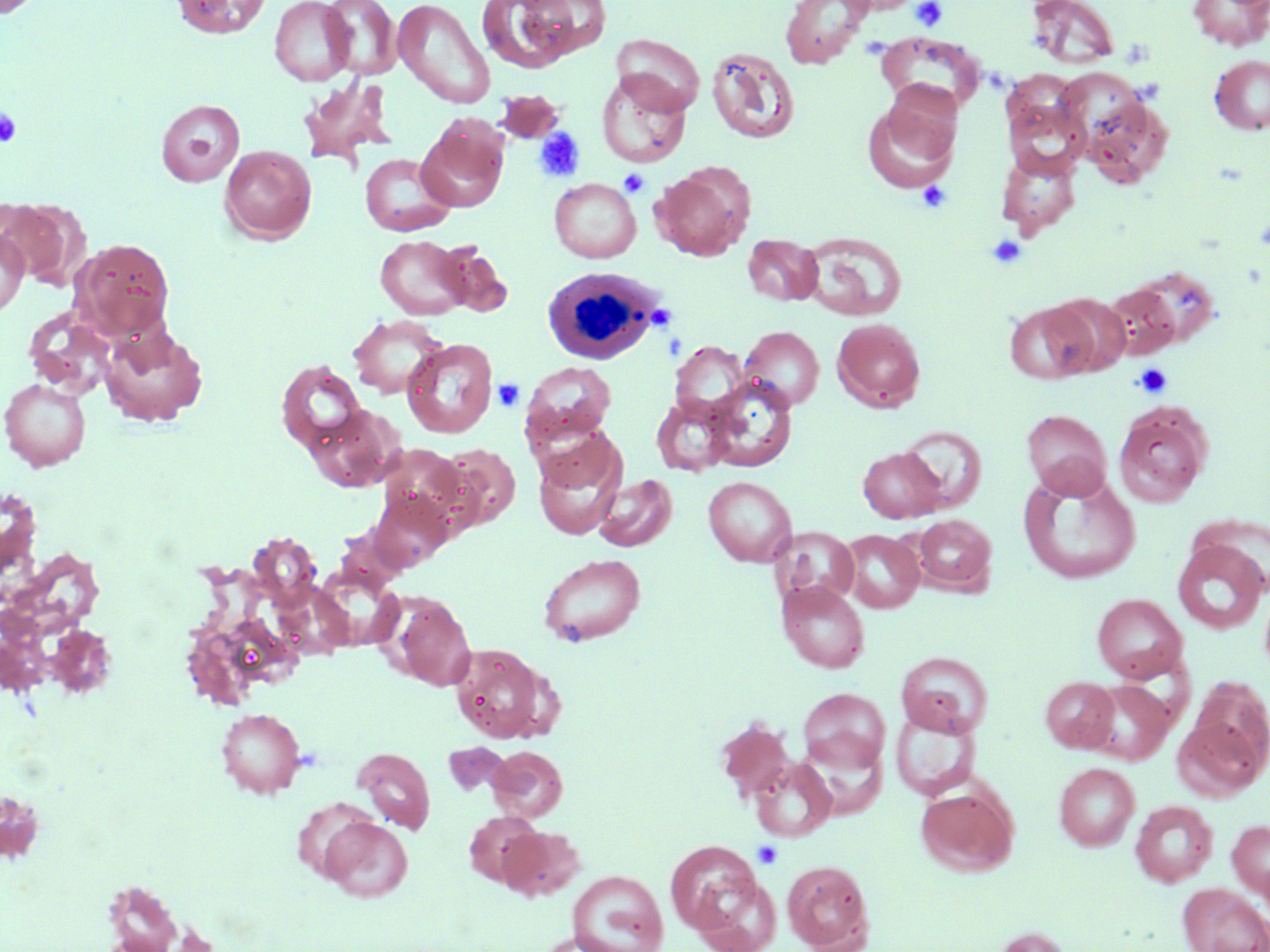

Summary:
  - Coordinate format: approximate bounding boxes as named x1/y1/x2/y2 corners in pixels
  - Uninfected red blood cell locations (subset): (x1=171, y1=0, x2=270, y2=38), (x1=321, y1=0, x2=401, y2=80), (x1=393, y1=0, x2=495, y2=109), (x1=476, y1=0, x2=585, y2=73), (x1=781, y1=0, x2=873, y2=68), (x1=840, y1=0, x2=922, y2=14), (x1=1026, y1=0, x2=1119, y2=70), (x1=1188, y1=0, x2=1270, y2=51), (x1=269, y1=1, x2=355, y2=86), (x1=876, y1=32, x2=983, y2=116), (x1=612, y1=34, x2=704, y2=115), (x1=706, y1=46, x2=800, y2=144), (x1=1209, y1=55, x2=1270, y2=135), (x1=596, y1=70, x2=692, y2=167), (x1=298, y1=76, x2=399, y2=168), (x1=494, y1=90, x2=564, y2=144), (x1=862, y1=92, x2=960, y2=192), (x1=1078, y1=93, x2=1174, y2=188), (x1=1003, y1=97, x2=1088, y2=180), (x1=156, y1=99, x2=245, y2=187), (x1=416, y1=116, x2=509, y2=212), (x1=220, y1=145, x2=316, y2=244), (x1=996, y1=150, x2=1081, y2=239), (x1=360, y1=153, x2=454, y2=237), (x1=651, y1=167, x2=752, y2=260), (x1=550, y1=178, x2=641, y2=263), (x1=0, y1=229, x2=28, y2=317), (x1=801, y1=232, x2=908, y2=321), (x1=375, y1=234, x2=471, y2=319), (x1=743, y1=234, x2=823, y2=305), (x1=72, y1=238, x2=175, y2=341), (x1=434, y1=242, x2=513, y2=318), (x1=1102, y1=284, x2=1180, y2=360), (x1=1047, y1=292, x2=1132, y2=376), (x1=1005, y1=301, x2=1096, y2=384), (x1=23, y1=309, x2=116, y2=398), (x1=348, y1=315, x2=448, y2=399), (x1=832, y1=318, x2=925, y2=412), (x1=100, y1=323, x2=208, y2=427), (x1=739, y1=326, x2=824, y2=412), (x1=401, y1=338, x2=498, y2=438), (x1=670, y1=342, x2=748, y2=420), (x1=275, y1=359, x2=368, y2=455), (x1=519, y1=360, x2=617, y2=448), (x1=704, y1=376, x2=797, y2=472), (x1=0, y1=378, x2=91, y2=471), (x1=651, y1=395, x2=734, y2=476), (x1=1114, y1=403, x2=1213, y2=508), (x1=306, y1=404, x2=403, y2=492), (x1=1022, y1=409, x2=1112, y2=499), (x1=900, y1=423, x2=986, y2=510), (x1=533, y1=437, x2=627, y2=540), (x1=437, y1=445, x2=520, y2=531), (x1=375, y1=446, x2=473, y2=531), (x1=857, y1=446, x2=945, y2=523), (x1=1018, y1=472, x2=1141, y2=584), (x1=593, y1=474, x2=678, y2=552), (x1=703, y1=476, x2=797, y2=566), (x1=367, y1=489, x2=454, y2=572), (x1=912, y1=514, x2=996, y2=595), (x1=774, y1=527, x2=859, y2=607), (x1=840, y1=530, x2=924, y2=613), (x1=1172, y1=538, x2=1268, y2=634), (x1=537, y1=553, x2=646, y2=646), (x1=314, y1=568, x2=405, y2=651), (x1=1259, y1=578, x2=1270, y2=683), (x1=777, y1=581, x2=870, y2=673), (x1=386, y1=593, x2=476, y2=691), (x1=1091, y1=593, x2=1187, y2=683), (x1=450, y1=644, x2=553, y2=743), (x1=896, y1=652, x2=993, y2=737), (x1=1040, y1=676, x2=1119, y2=753), (x1=1188, y1=677, x2=1270, y2=775), (x1=1081, y1=679, x2=1175, y2=765), (x1=798, y1=688, x2=891, y2=773), (x1=890, y1=707, x2=981, y2=800), (x1=217, y1=708, x2=305, y2=798), (x1=1173, y1=713, x2=1266, y2=801), (x1=798, y1=730, x2=887, y2=819), (x1=487, y1=745, x2=568, y2=823), (x1=352, y1=747, x2=435, y2=833), (x1=750, y1=757, x2=836, y2=842), (x1=1053, y1=763, x2=1139, y2=851), (x1=915, y1=784, x2=1018, y2=877), (x1=292, y1=798, x2=380, y2=882), (x1=1130, y1=800, x2=1218, y2=887), (x1=464, y1=811, x2=544, y2=886), (x1=321, y1=816, x2=413, y2=902), (x1=1227, y1=818, x2=1270, y2=902), (x1=498, y1=825, x2=585, y2=901), (x1=665, y1=839, x2=769, y2=941), (x1=782, y1=860, x2=874, y2=951), (x1=567, y1=870, x2=668, y2=952), (x1=100, y1=877, x2=184, y2=952), (x1=1178, y1=883, x2=1270, y2=952), (x1=990, y1=926, x2=1073, y2=952), (x1=531, y1=934, x2=626, y2=952)
  - Platelet locations (subset): (x1=911, y1=0, x2=947, y2=31), (x1=0, y1=107, x2=22, y2=148), (x1=534, y1=127, x2=585, y2=183), (x1=619, y1=169, x2=649, y2=197), (x1=917, y1=181, x2=952, y2=214), (x1=986, y1=235, x2=1027, y2=268), (x1=1133, y1=363, x2=1172, y2=398), (x1=492, y1=378, x2=525, y2=411), (x1=753, y1=840, x2=783, y2=868)
  - White blood cell locations: (x1=549, y1=262, x2=669, y2=361)
  - Slide-level diagnosis: negative for blood parasites
  - Preparation: thin blood smear
  - Stain: May-Grünwald-Giemsa
  - Magnification: 1000x
  - Image size: 1270×952 pixels
  - Modality: light microscopy
  - Field of view: single